Report the malaria status of this cell.
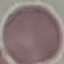

It is uninfected.

{
  "image_type": "cell patch, automatically extracted from a larger field of view and resized to 64 × 64 pixels",
  "capture": "smartphone camera at the microscope eyepiece",
  "stain": "Giemsa",
  "preparation": "thin blood smear"
}